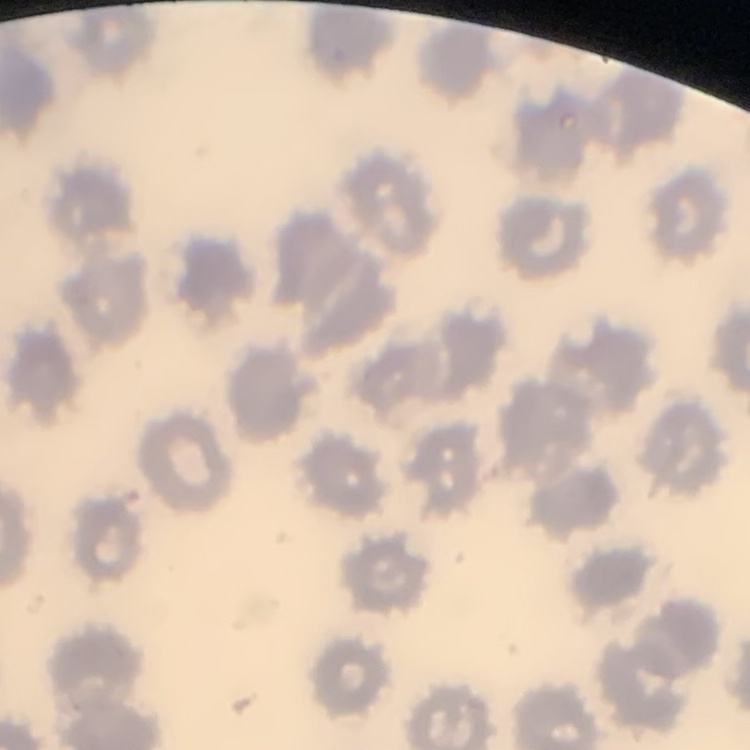
The erythrocytes exhibit no rouleaux formation. Square crop of a larger photomicrograph. Thin peripheral smear. Field's or Giemsa stain.